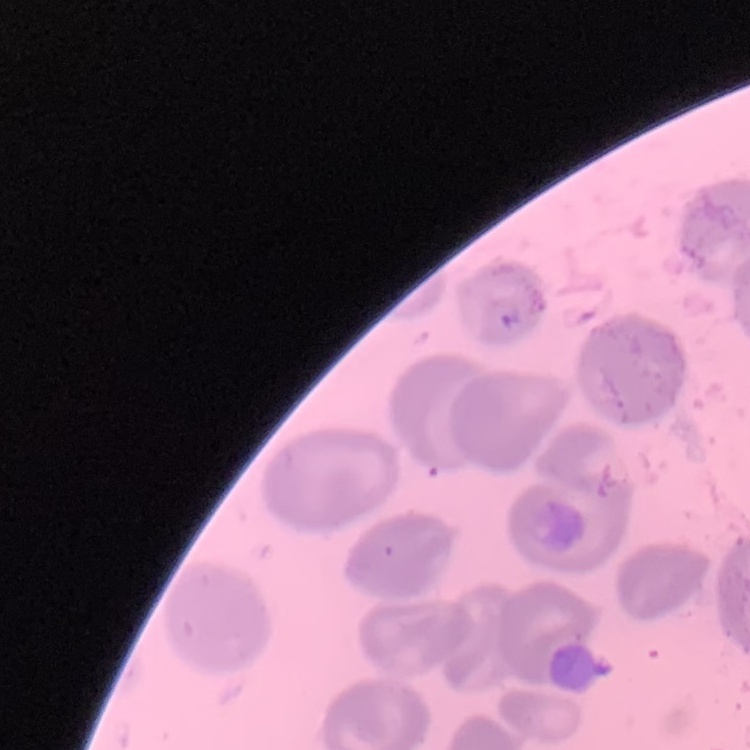 The erythrocytes exhibit no rouleaux formation. One tile cut from a larger photomicrograph. Thin peripheral smear. Field's or Giemsa stain.